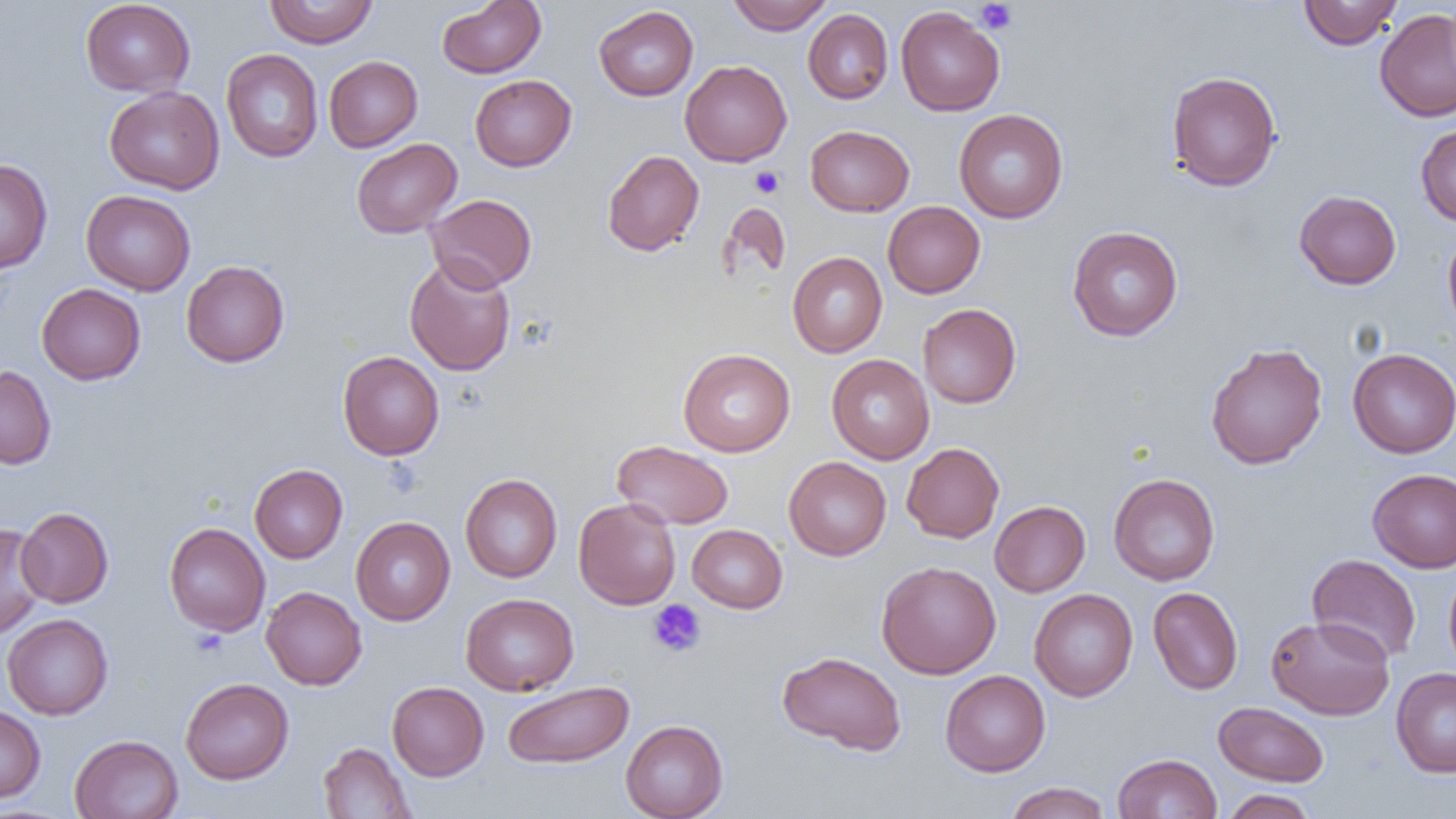
Summary:
  - Coordinate format: approximate bounding boxes as [x1, y1, x2, y2] in pixels
  - Platelet locations: [975, 1, 1017, 34], [751, 166, 784, 198], [648, 599, 706, 657], [191, 627, 229, 658]
  - Uninfected red blood cell locations: [80, 0, 195, 96], [265, 0, 378, 48], [728, 0, 834, 34], [1298, 0, 1403, 50], [436, 1, 546, 78], [594, 5, 699, 101], [896, 7, 1005, 116], [1374, 8, 1456, 122], [803, 9, 893, 104], [222, 49, 323, 162], [324, 55, 422, 152], [680, 60, 792, 166], [1166, 70, 1281, 192], [469, 74, 577, 171], [104, 86, 224, 194], [954, 109, 1068, 223], [1415, 124, 1456, 225], [805, 125, 914, 217], [351, 138, 462, 238], [602, 150, 704, 256], [0, 158, 52, 274], [81, 190, 195, 295], [1294, 190, 1401, 290], [425, 194, 537, 292], [883, 201, 985, 298], [718, 202, 791, 283], [1067, 225, 1183, 341], [1443, 229, 1456, 335], [788, 252, 887, 357], [404, 256, 516, 376], [181, 260, 290, 367], [36, 283, 146, 385], [918, 303, 1021, 408], [1205, 342, 1328, 469], [1347, 348, 1456, 458], [678, 349, 795, 456], [338, 351, 444, 460], [826, 354, 935, 464], [0, 365, 57, 469], [612, 440, 733, 529], [902, 443, 1004, 543], [784, 456, 891, 560], [249, 464, 348, 563], [1368, 468, 1456, 572], [1108, 473, 1220, 585], [460, 474, 562, 582], [574, 498, 681, 609], [990, 501, 1090, 596], [16, 507, 113, 608], [351, 517, 455, 625], [164, 522, 270, 636], [0, 524, 45, 639], [687, 524, 787, 613], [1307, 553, 1421, 664], [876, 561, 1001, 679], [1444, 566, 1456, 676], [261, 586, 367, 690], [1148, 587, 1243, 695], [1029, 589, 1138, 701], [461, 593, 578, 696], [2, 614, 113, 720], [1266, 615, 1395, 720], [776, 650, 907, 756], [1391, 667, 1456, 778], [940, 670, 1050, 776], [180, 677, 293, 784], [387, 681, 489, 780], [502, 681, 634, 769], [1214, 701, 1329, 786], [0, 705, 46, 803], [620, 720, 728, 819], [70, 734, 183, 818], [318, 742, 416, 818], [1112, 753, 1222, 818], [1003, 782, 1112, 819], [1220, 789, 1317, 819]
  - Slide-level diagnosis: no evidence of blood parasites
  - Field of view: one of a larger specimen
  - Modality: light microscopy
  - Magnification: 1000x
  - Preparation: thin blood film
  - Image size: 1456×819 pixels